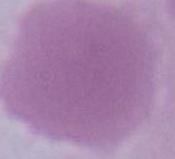
magnification: 1000x
identification: red blood cell
modality: photomicrograph